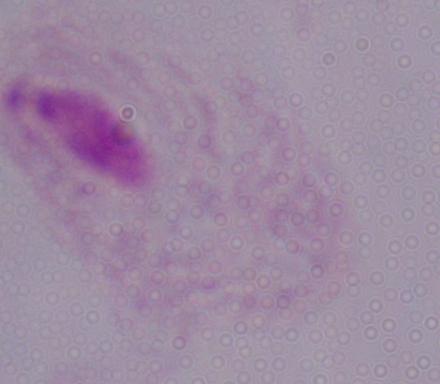

Summary:
  - Magnification: 1000x
  - Identification: trichomonad
  - Modality: photomicrograph